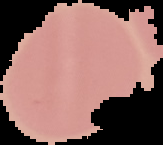
Summary:
  - Image size: 163×145 pixels
  - Preparation: thin blood smear
  - Image type: segmented cell region on a black background
  - Malaria status: uninfected